Look for Plasmodium parasites.
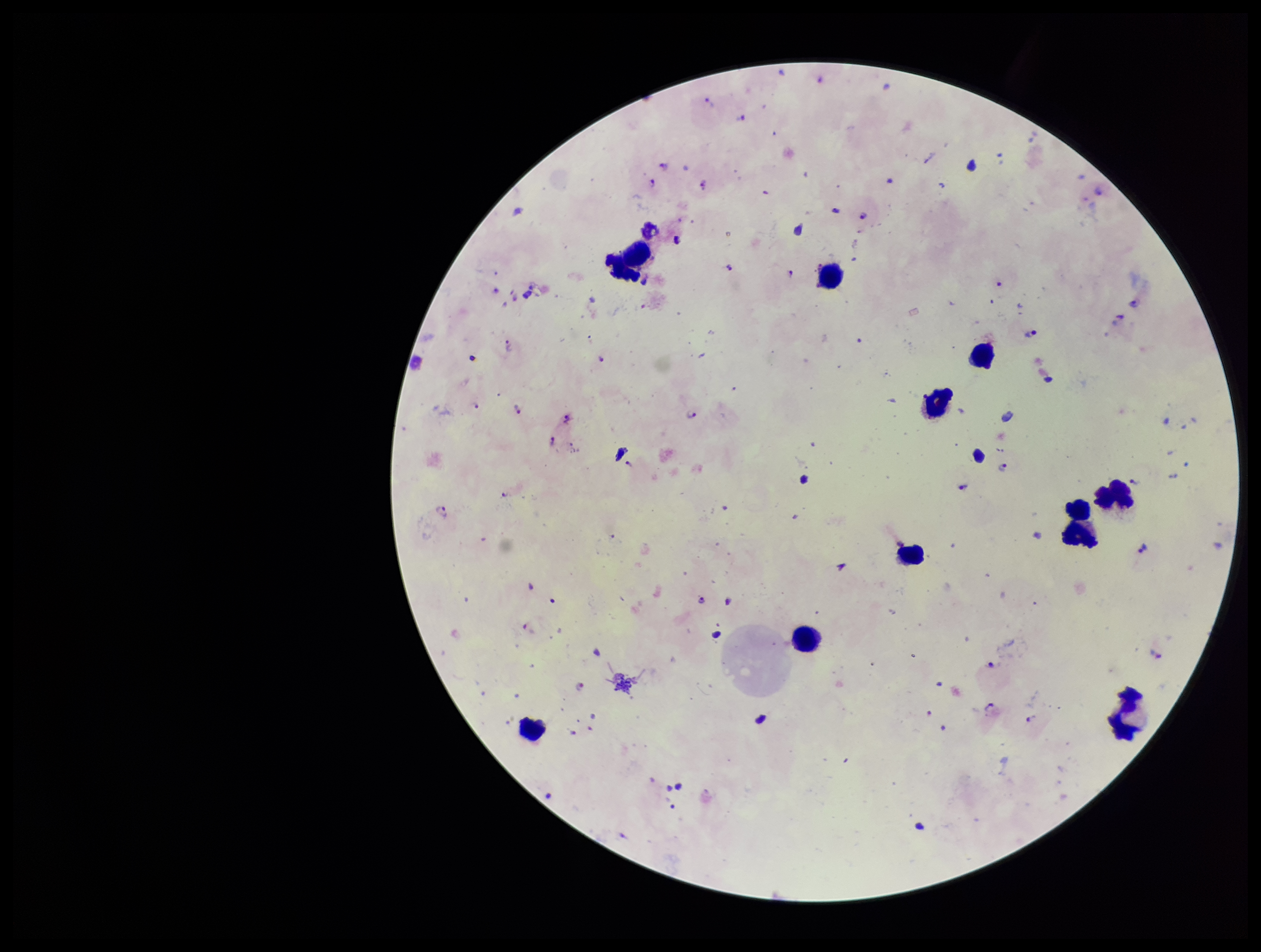
Detected.

Summary:
  - Preparation: thick smear
  - Leukocyte count: 11
  - Field of view: single
  - Parasite count: 50
  - Species reported for this patient: Plasmodium falciparum
  - Capture: smartphone photograph through the microscope eyepiece
  - Stain: Giemsa
  - Patient malaria status: infected
  - Image size: 1261×952 pixels